Describe the morphology of the erythrocytes.
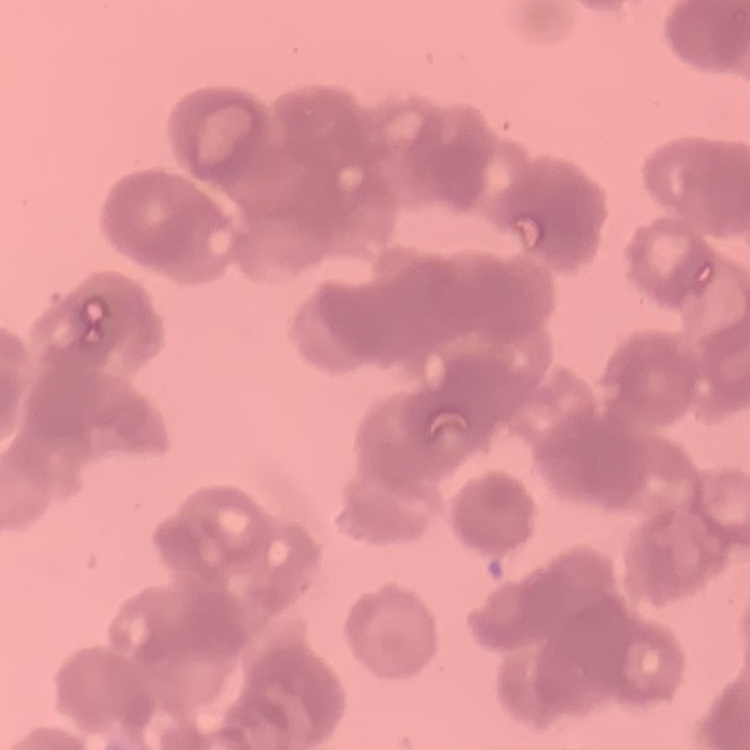

Rouleaux formation.

Summary:
  - Image type: square crop of a larger photomicrograph
  - Stain: Field's or Giemsa
  - Preparation: thin blood film